Report the malaria status of this cell.
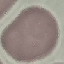
Uninfected.

Summary:
  - Image type: automatically extracted cell patch, resized to 64 × 64 pixels
  - Stain: Giemsa
  - Preparation: thin blood smear
  - Capture: smartphone camera at the microscope eyepiece